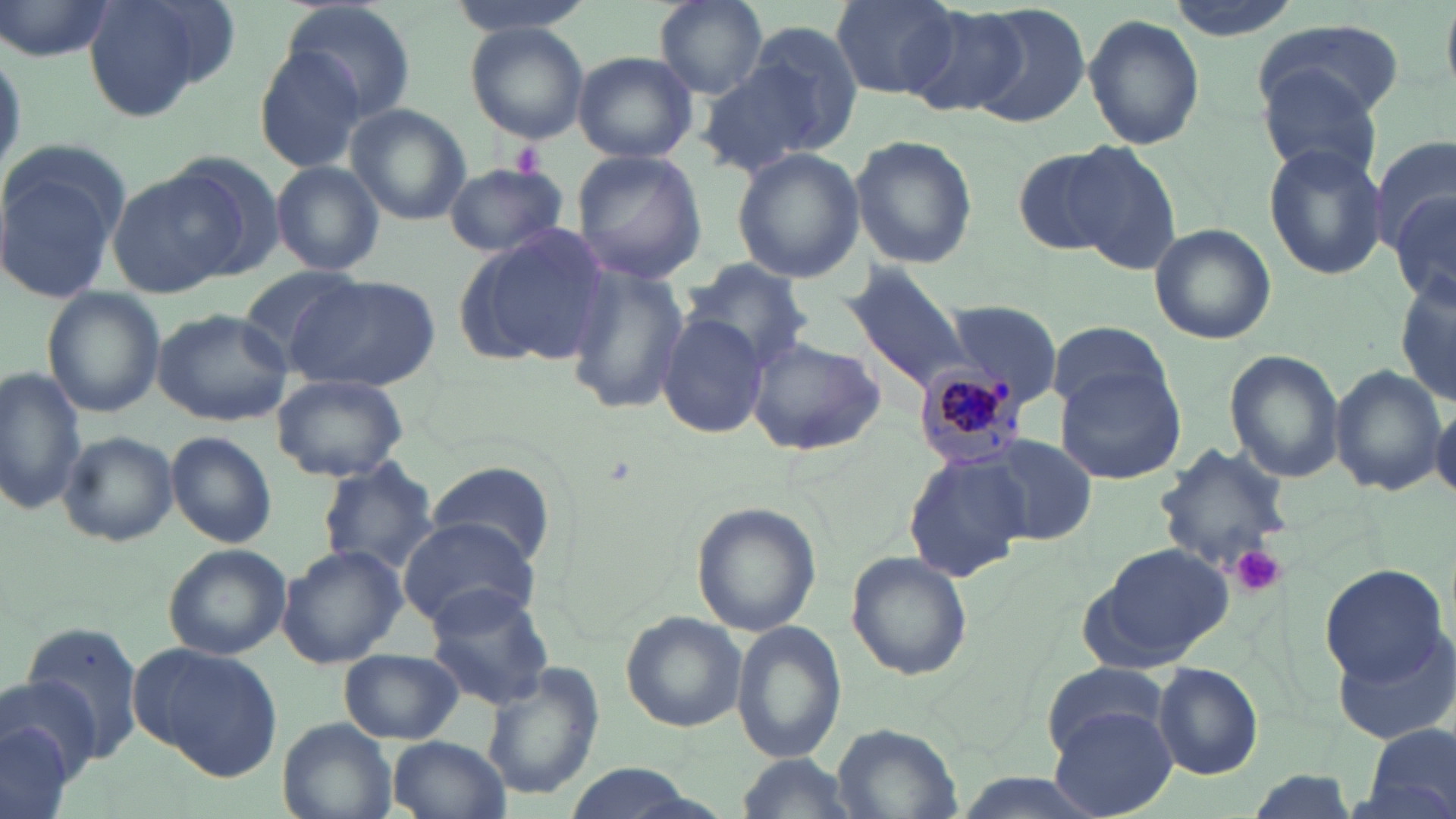
Approximate bounding boxes as [x1, y1, x2, y2] in pixels. Plasmodium malariae-infected red blood cell locations: [911, 365, 1026, 470]. Platelet locations: [510, 140, 543, 177], [1228, 544, 1287, 597]. Uninfected red blood cell locations: [0, 0, 114, 62], [81, 0, 238, 123], [281, 0, 415, 124], [449, 0, 594, 36], [655, 0, 769, 98], [832, 0, 960, 99], [902, 4, 1030, 118], [966, 4, 1092, 129], [1083, 15, 1205, 150], [1252, 18, 1405, 123], [467, 24, 590, 143], [701, 33, 859, 173], [251, 44, 369, 174], [573, 51, 699, 166], [1257, 69, 1385, 185], [346, 105, 472, 225], [1372, 132, 1456, 256], [850, 134, 978, 267], [0, 140, 132, 302], [1063, 142, 1184, 276], [1264, 143, 1389, 281], [1012, 146, 1137, 259], [730, 148, 864, 284], [163, 150, 289, 280], [570, 150, 707, 284], [269, 160, 384, 277], [442, 163, 568, 257], [110, 170, 243, 297], [1389, 191, 1456, 310], [1148, 223, 1277, 346], [458, 227, 612, 364], [563, 260, 690, 414], [684, 260, 814, 373], [843, 264, 980, 403], [239, 266, 365, 366], [284, 274, 442, 392], [1395, 274, 1455, 408], [41, 286, 165, 418], [943, 298, 1065, 408], [152, 307, 295, 426], [659, 313, 770, 440], [1045, 321, 1171, 415], [745, 337, 883, 457], [1224, 351, 1344, 483], [0, 364, 86, 518], [1053, 365, 1190, 483], [1330, 365, 1448, 496], [271, 373, 409, 482], [1430, 403, 1456, 502], [58, 431, 179, 545], [167, 431, 279, 548], [981, 437, 1098, 546], [1152, 442, 1297, 580], [902, 453, 1029, 582], [315, 458, 439, 576], [427, 460, 555, 565], [692, 502, 819, 637], [399, 516, 540, 629], [1086, 541, 1236, 669], [161, 543, 293, 658], [276, 543, 407, 668], [845, 552, 972, 681], [1318, 563, 1448, 684], [424, 580, 554, 709], [622, 612, 745, 733], [17, 617, 147, 772], [730, 620, 847, 764], [1331, 627, 1456, 745], [131, 643, 283, 781], [340, 647, 464, 744], [1041, 660, 1170, 761], [478, 662, 605, 804], [1152, 662, 1263, 781], [1, 685, 93, 817], [1049, 706, 1179, 818], [277, 718, 397, 819], [1358, 722, 1456, 816], [829, 725, 965, 818], [386, 736, 508, 818], [731, 752, 862, 819], [560, 763, 709, 819]. Slide-level diagnosis: Plasmodium malariae. 1000x magnification. Image is 1456×819 pixels. Optical microscopy. May-Grünwald-Giemsa stain. Single field of view. Thin blood film.